Assess this cell for malaria.
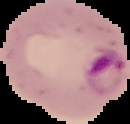
It is parasitized.

Summary:
  - Image size: 130×124 pixels
  - Image type: cell region segmented out of the field of view; surrounding area masked to black
  - Preparation: thin blood film